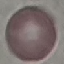
{
  "malaria_status": "uninfected",
  "capture": "smartphone camera at the microscope eyepiece",
  "image_type": "cell patch, automatically extracted from a larger field of view and resized to 64 × 64 pixels",
  "stain": "Giemsa",
  "preparation": "thin blood film"
}